Assess this cell for malaria.
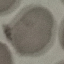
It is uninfected.

stain: Giemsa
image_type: cell patch, automatically extracted from a larger field of view and resized to 64 × 64 pixels
capture: smartphone through the microscope eyepiece
preparation: thin blood smear